Assess this cell for malaria.
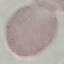
It is uninfected.

Automatically extracted cell patch, resized to 64 × 64 pixels. Thin blood film. Acquired by smartphone through the microscope eyepiece. Giemsa stain.